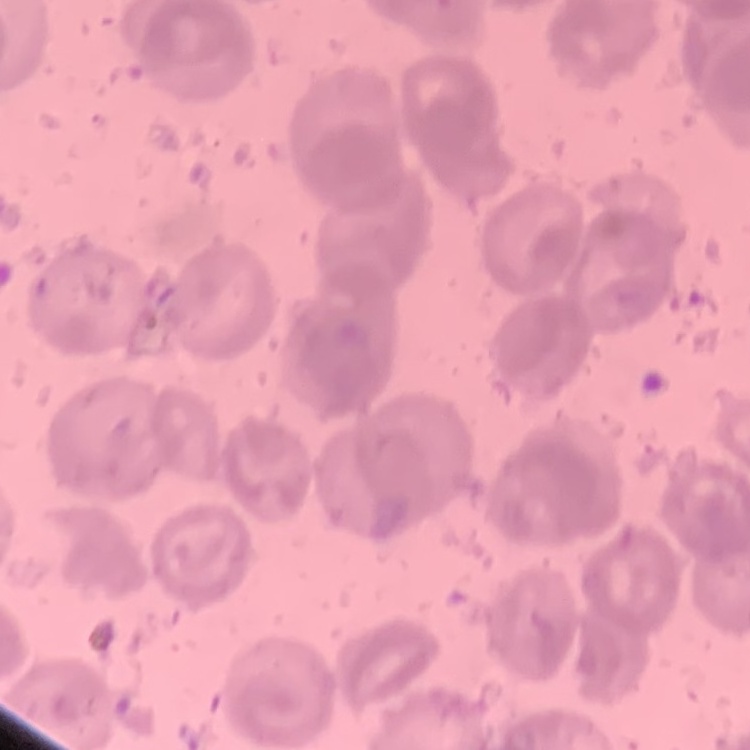

The erythrocytes exhibit no rouleaux formation. Square crop of a larger photomicrograph. Field's or Giemsa stain. Thin blood film.